State the blood parasite species.
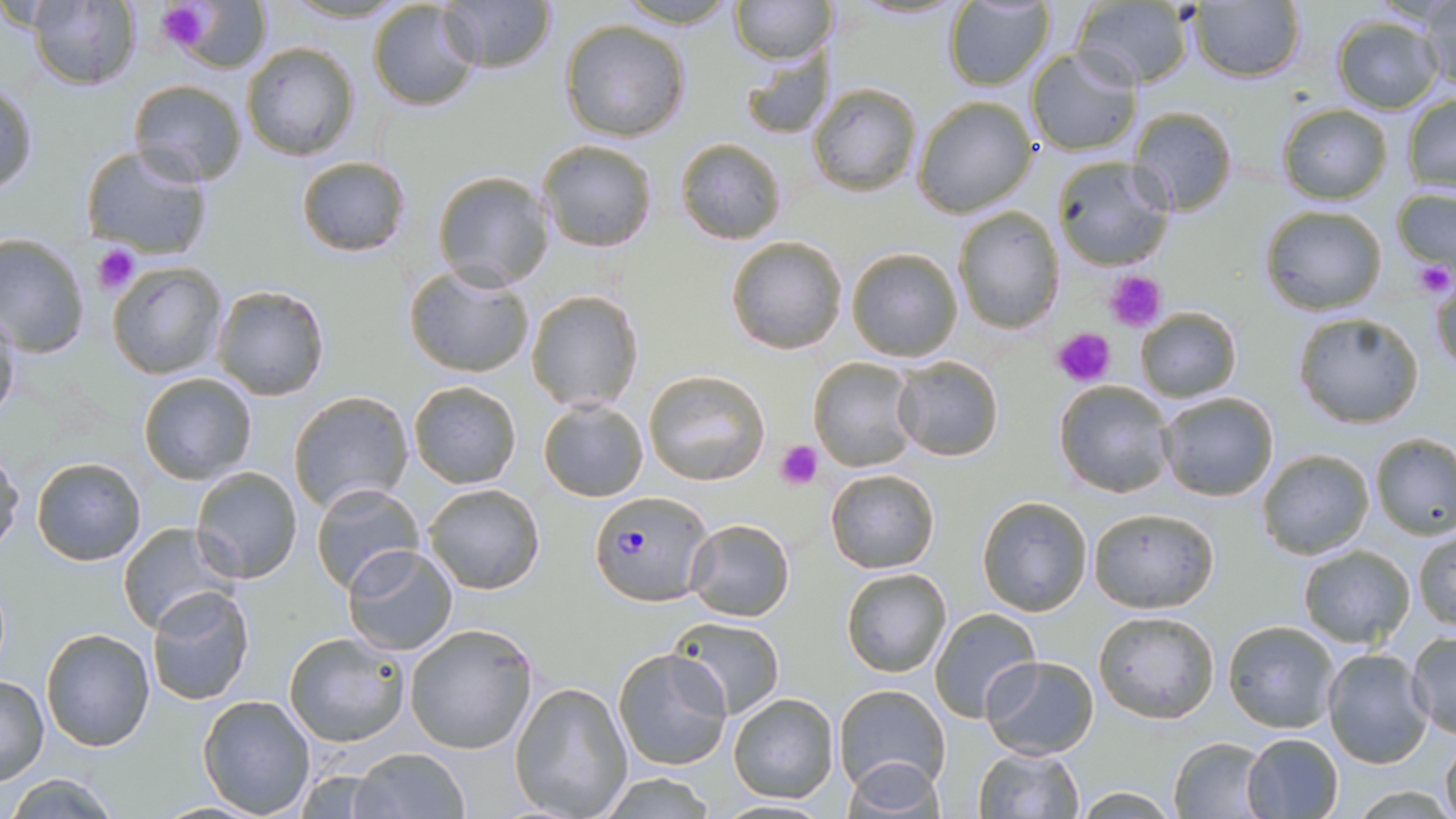

Plasmodium falciparum.

image size = 1456×819 pixels
stain = May-Grünwald-Giemsa
modality = light microscopy
field of view = single
platelet locations = approximate bounding boxes as named x1/y1/x2/y2 corners in pixels: (x1=155, y1=2, x2=216, y2=55), (x1=92, y1=243, x2=140, y2=295), (x1=1412, y1=260, x2=1454, y2=297), (x1=1107, y1=269, x2=1166, y2=334), (x1=1050, y1=327, x2=1116, y2=387), (x1=775, y1=440, x2=824, y2=491)
magnification = 1000x
preparation = thin blood film
uninfected red blood cell locations = approximate bounding boxes as named x1/y1/x2/y2 corners in pixels: (x1=439, y1=0, x2=558, y2=74), (x1=614, y1=0, x2=742, y2=29), (x1=730, y1=0, x2=835, y2=64), (x1=1188, y1=0, x2=1307, y2=83), (x1=25, y1=1, x2=142, y2=89), (x1=170, y1=1, x2=273, y2=73), (x1=368, y1=1, x2=483, y2=112), (x1=942, y1=2, x2=1056, y2=88), (x1=1071, y1=2, x2=1196, y2=87), (x1=1412, y1=2, x2=1456, y2=90), (x1=1331, y1=15, x2=1442, y2=113), (x1=560, y1=19, x2=690, y2=142), (x1=241, y1=42, x2=361, y2=162), (x1=1025, y1=45, x2=1143, y2=155), (x1=739, y1=46, x2=833, y2=140), (x1=129, y1=79, x2=249, y2=187), (x1=1, y1=80, x2=37, y2=199), (x1=808, y1=82, x2=922, y2=195), (x1=1402, y1=92, x2=1456, y2=192), (x1=913, y1=96, x2=1037, y2=218), (x1=1276, y1=104, x2=1392, y2=204), (x1=1128, y1=106, x2=1238, y2=216), (x1=536, y1=138, x2=659, y2=252), (x1=675, y1=138, x2=787, y2=244), (x1=79, y1=145, x2=213, y2=261), (x1=295, y1=154, x2=412, y2=257), (x1=1052, y1=156, x2=1176, y2=270), (x1=432, y1=169, x2=555, y2=291), (x1=1389, y1=186, x2=1456, y2=276), (x1=1258, y1=204, x2=1386, y2=314), (x1=953, y1=206, x2=1064, y2=333), (x1=0, y1=234, x2=91, y2=359), (x1=725, y1=235, x2=850, y2=354), (x1=846, y1=247, x2=963, y2=363), (x1=106, y1=262, x2=228, y2=379), (x1=403, y1=264, x2=535, y2=379), (x1=1429, y1=268, x2=1456, y2=382), (x1=211, y1=284, x2=332, y2=402), (x1=524, y1=290, x2=643, y2=412), (x1=1134, y1=306, x2=1241, y2=403), (x1=0, y1=307, x2=21, y2=428), (x1=1293, y1=311, x2=1425, y2=428), (x1=892, y1=355, x2=1004, y2=461), (x1=809, y1=356, x2=918, y2=472), (x1=645, y1=369, x2=770, y2=486), (x1=138, y1=371, x2=258, y2=485), (x1=407, y1=379, x2=522, y2=488), (x1=1053, y1=379, x2=1176, y2=498), (x1=289, y1=390, x2=414, y2=512), (x1=1156, y1=391, x2=1279, y2=500), (x1=536, y1=398, x2=649, y2=503), (x1=1369, y1=433, x2=1456, y2=538), (x1=0, y1=449, x2=23, y2=554), (x1=1257, y1=449, x2=1374, y2=559), (x1=30, y1=455, x2=146, y2=566), (x1=191, y1=466, x2=302, y2=583), (x1=825, y1=469, x2=941, y2=573), (x1=311, y1=482, x2=424, y2=595), (x1=423, y1=483, x2=545, y2=596), (x1=977, y1=495, x2=1093, y2=616), (x1=1088, y1=508, x2=1219, y2=613), (x1=685, y1=518, x2=795, y2=621), (x1=117, y1=521, x2=237, y2=634), (x1=1412, y1=528, x2=1456, y2=632), (x1=1296, y1=545, x2=1415, y2=649), (x1=341, y1=546, x2=458, y2=656), (x1=841, y1=567, x2=952, y2=678), (x1=145, y1=586, x2=257, y2=705), (x1=929, y1=608, x2=1040, y2=721), (x1=1094, y1=611, x2=1221, y2=725), (x1=669, y1=617, x2=785, y2=718), (x1=1222, y1=619, x2=1340, y2=734), (x1=404, y1=623, x2=539, y2=756), (x1=41, y1=627, x2=155, y2=752), (x1=284, y1=630, x2=411, y2=749), (x1=1406, y1=630, x2=1455, y2=739), (x1=1255, y1=636, x2=1398, y2=752), (x1=612, y1=646, x2=734, y2=771), (x1=1321, y1=646, x2=1430, y2=768), (x1=980, y1=655, x2=1099, y2=759), (x1=0, y1=673, x2=49, y2=785), (x1=511, y1=680, x2=633, y2=817), (x1=834, y1=683, x2=950, y2=795), (x1=727, y1=691, x2=840, y2=804), (x1=197, y1=694, x2=317, y2=817), (x1=1241, y1=731, x2=1344, y2=817), (x1=1168, y1=735, x2=1270, y2=817), (x1=1440, y1=736, x2=1455, y2=819), (x1=972, y1=746, x2=1085, y2=819), (x1=353, y1=747, x2=468, y2=818), (x1=840, y1=757, x2=946, y2=818), (x1=290, y1=769, x2=394, y2=817), (x1=5, y1=772, x2=123, y2=818), (x1=595, y1=772, x2=720, y2=818), (x1=1072, y1=787, x2=1178, y2=816), (x1=711, y1=799, x2=838, y2=817)
Plasmodium falciparum-infected red blood cell locations = approximate bounding boxes as named x1/y1/x2/y2 corners in pixels: (x1=587, y1=490, x2=711, y2=604)